Locate and identify every blood parasite.
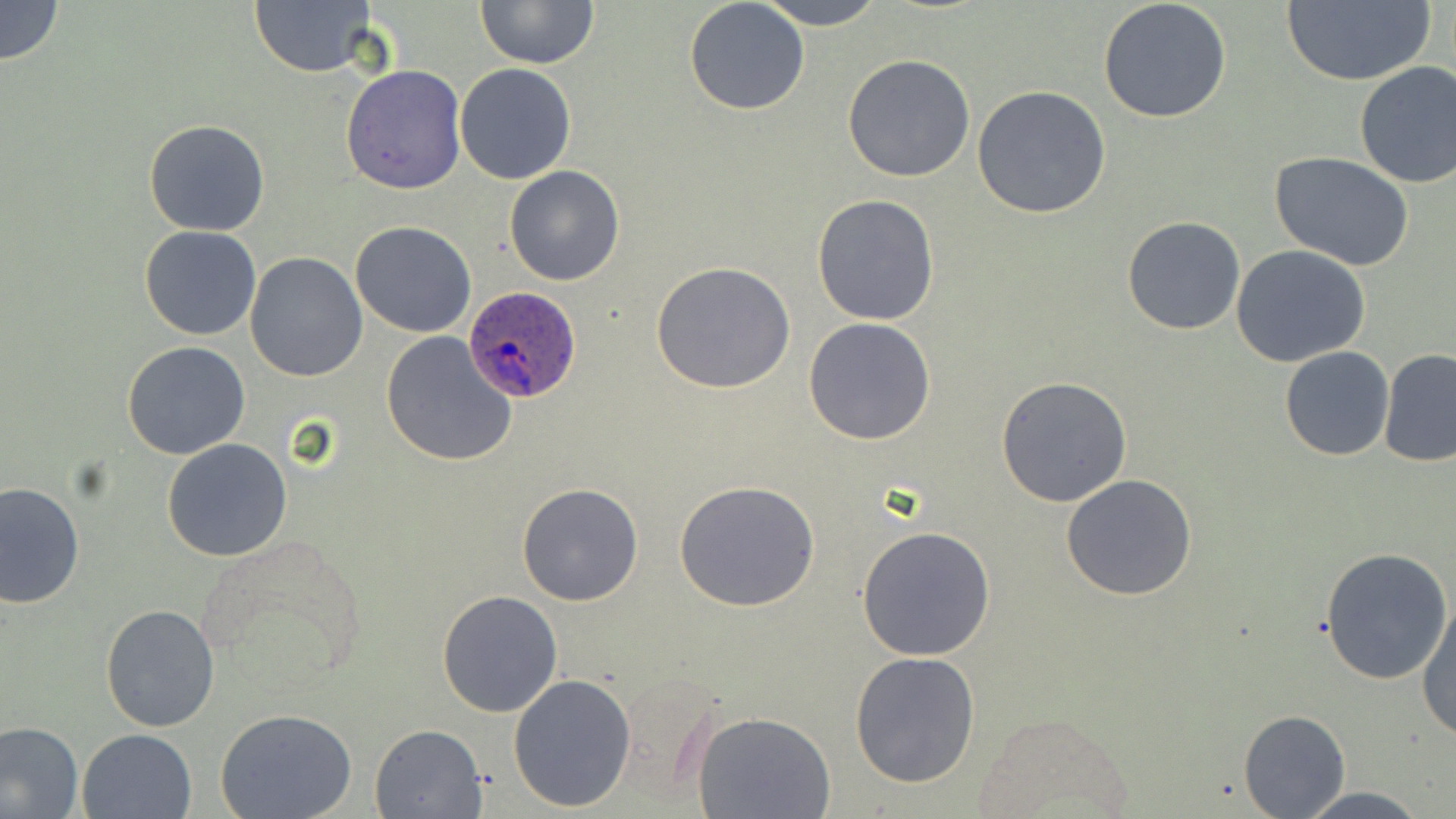

Approximate bounding boxes as (x1, y1, x2, y2) in pixels.
Plasmodium ovale-infected red blood cells: (461, 288, 584, 403).
No Plasmodium falciparum, Plasmodium malariae, Plasmodium vivax, Babesia divergens, or Trypanosoma brucei observed.

Uninfected red blood cell locations: (0, 0, 64, 65), (476, 0, 599, 68), (754, 0, 887, 29), (1097, 0, 1232, 123), (684, 1, 811, 115), (1280, 1, 1435, 85), (249, 2, 376, 77), (843, 55, 975, 182), (1354, 60, 1456, 190), (454, 63, 577, 184), (341, 64, 468, 195), (973, 85, 1111, 219), (144, 119, 271, 236), (1270, 151, 1415, 274), (504, 166, 624, 286), (811, 194, 942, 326), (1122, 216, 1248, 335), (350, 221, 476, 337), (140, 225, 262, 342), (135, 239, 366, 360), (1230, 245, 1372, 368), (244, 252, 368, 382), (652, 262, 795, 395), (803, 317, 937, 445), (380, 331, 519, 467), (122, 341, 251, 460), (1279, 345, 1392, 462), (1379, 346, 1456, 469), (995, 375, 1135, 507), (162, 439, 293, 560), (1061, 474, 1197, 601), (675, 480, 822, 613), (0, 482, 84, 608), (516, 482, 644, 607), (857, 526, 996, 661), (1319, 547, 1454, 686), (437, 590, 564, 718), (1415, 596, 1456, 742), (101, 604, 221, 732), (849, 651, 981, 788), (508, 673, 636, 812), (1239, 709, 1349, 817), (216, 710, 358, 819), (973, 710, 1137, 817), (691, 711, 837, 819), (0, 721, 83, 818), (371, 723, 487, 817), (79, 728, 198, 819), (1297, 787, 1432, 819). Slide-level diagnosis: Plasmodium ovale. Optical microscopy. May-Grünwald-Giemsa stain. One field of a larger specimen. Image is 1456×819 pixels. 1000x magnification. Thin blood film.